Find each white blood cell.
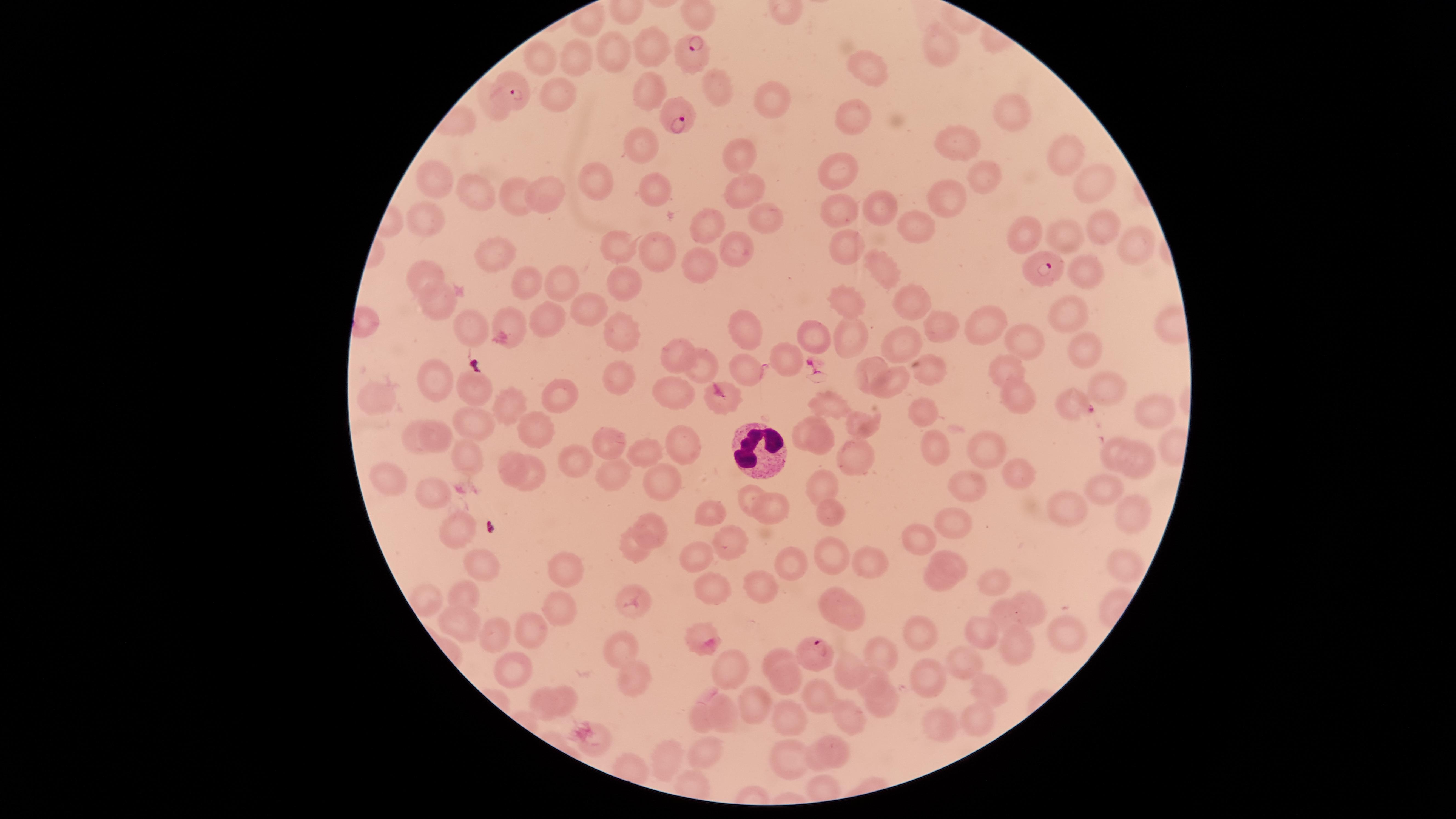
No white blood cells identified.

Approximate marker points as [x, y] in pixels. Uninfected red blood cells: [651, 43], [608, 45], [944, 45], [541, 59], [578, 59], [870, 67], [719, 85], [644, 87], [548, 91], [768, 97], [1008, 109], [844, 117], [958, 144], [641, 145], [1064, 148], [737, 151], [836, 169], [1090, 170], [980, 175], [597, 179], [441, 180], [656, 187], [739, 189], [518, 190], [546, 190], [478, 194], [944, 194], [875, 208], [833, 209], [770, 218], [709, 220], [427, 221], [914, 222], [1020, 224], [1098, 224], [1067, 233], [732, 242], [1125, 242], [851, 245], [615, 247], [653, 252], [495, 258], [879, 262], [698, 268], [1089, 269], [421, 270], [622, 278], [557, 281], [529, 282], [433, 290], [909, 293], [852, 302], [591, 305], [1061, 309], [546, 315], [467, 317], [508, 319], [980, 323], [740, 324], [942, 324], [620, 325], [812, 329], [1023, 335], [847, 338], [1082, 340], [909, 341], [678, 356], [708, 363], [746, 363], [785, 363], [1003, 366], [611, 367], [870, 367], [433, 382], [896, 385], [678, 388], [1115, 388], [467, 389], [563, 395], [375, 396], [827, 396], [1018, 398], [510, 401], [1070, 401], [1149, 409], [925, 413], [470, 417], [438, 422], [864, 422], [802, 424], [538, 425], [677, 435], [604, 437], [816, 443], [413, 446], [937, 447], [992, 447], [1113, 447], [640, 451], [464, 454], [849, 457], [574, 458], [508, 459], [1144, 460], [610, 470], [655, 472], [1021, 473], [529, 476], [388, 479], [825, 481], [968, 487], [1102, 487], [434, 491], [749, 493], [771, 502], [1068, 502], [831, 508], [707, 509], [1128, 517], [652, 519], [948, 522], [459, 530], [914, 532], [727, 536], [628, 544], [831, 550], [871, 557], [796, 558], [951, 560], [1124, 562], [697, 564], [560, 566], [480, 568], [757, 579], [715, 583], [993, 583], [941, 586], [426, 591], [834, 592], [471, 595], [631, 596], [1000, 605], [1026, 605], [558, 609], [852, 616], [459, 619], [989, 631], [1064, 631], [918, 632], [498, 633], [534, 633], [702, 636], [621, 644], [1023, 648], [780, 653], [883, 656], [965, 658], [727, 662], [843, 664], [519, 668], [630, 672], [871, 676], [781, 678], [930, 678], [984, 684], [817, 685], [569, 692], [749, 695], [886, 696], [726, 701], [544, 703], [843, 712], [792, 718], [703, 722], [979, 722], [933, 724], [589, 729], [829, 739], [709, 753], [790, 756], [666, 758], [813, 764]. Parasitized red blood cells: [693, 45], [513, 89], [670, 114], [1043, 268], [813, 649]. Thin blood smear. Species: Plasmodium falciparum. Presence: malaria parasites seen. Photographed with a smartphone camera through the microscope eyepiece. The visible region is circular. Giemsa-stained preparation. Image is 1456×819 pixels. One field of view of the specimen.